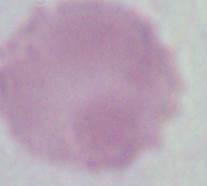

Summary:
  - Modality: photomicrograph
  - Identification: red blood cell
  - Magnification: 1000x